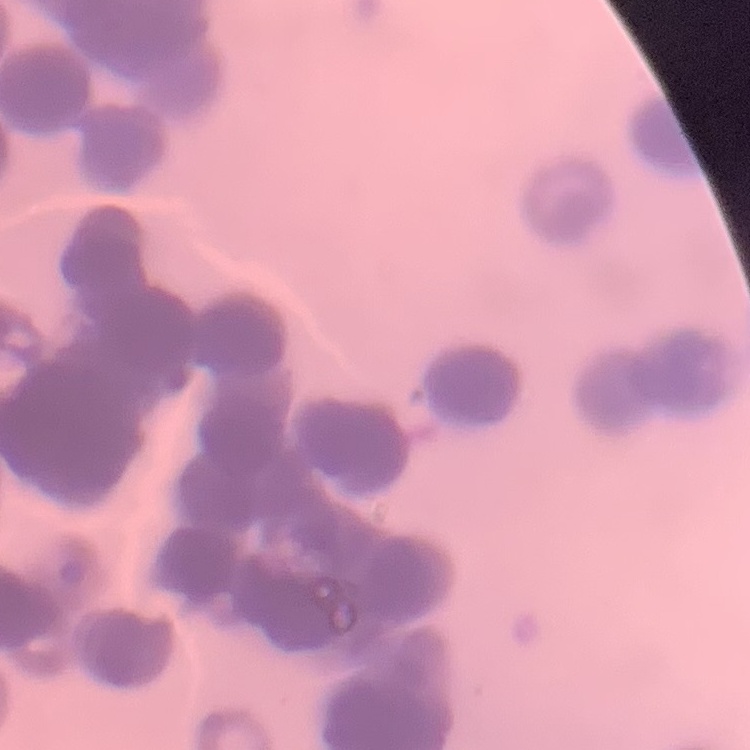
Summary:
  - Red blood cell morphology: rouleaux formation
  - Preparation: thin blood film
  - Stain: Field's or Giemsa
  - Image type: square crop of a larger photomicrograph